State which parasite is depicted.
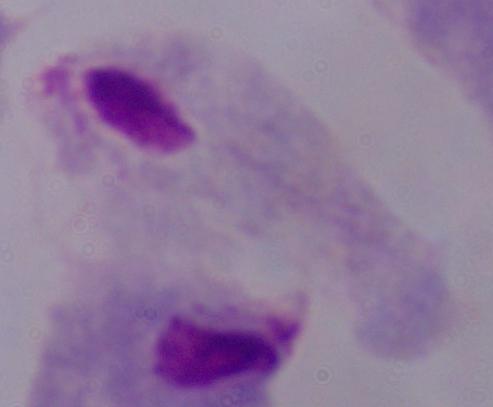

A trichomonad.

Micrograph. 1000x magnification.